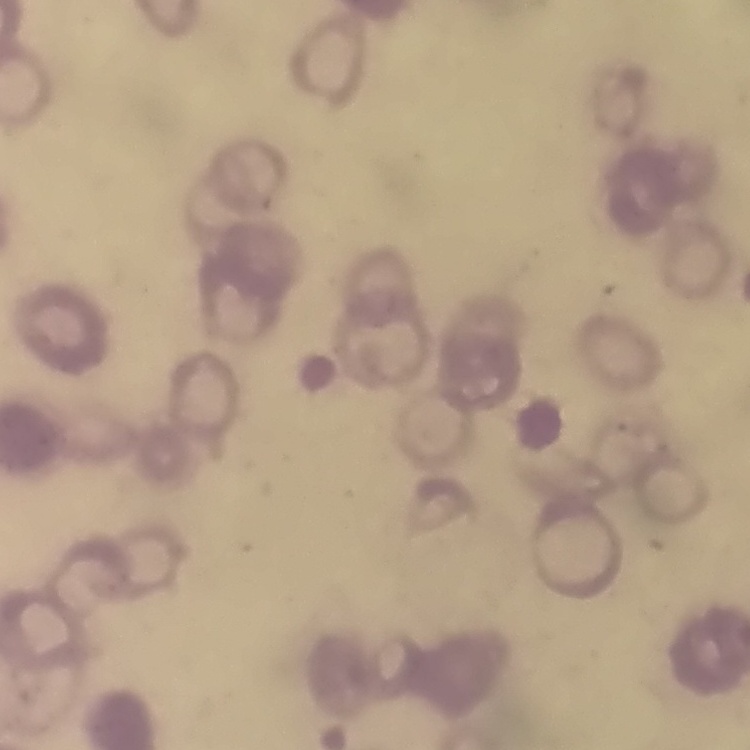
The red blood cells show rouleaux formation. Thin peripheral smear. One tile cut from a larger photomicrograph. Field's or Giemsa stain.